Assess this cell for malaria.
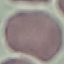

It is uninfected.

Giemsa stain. Acquired by smartphone through the microscope eyepiece. Thin blood film. Automatically extracted cell patch, resized to 64 × 64 pixels.